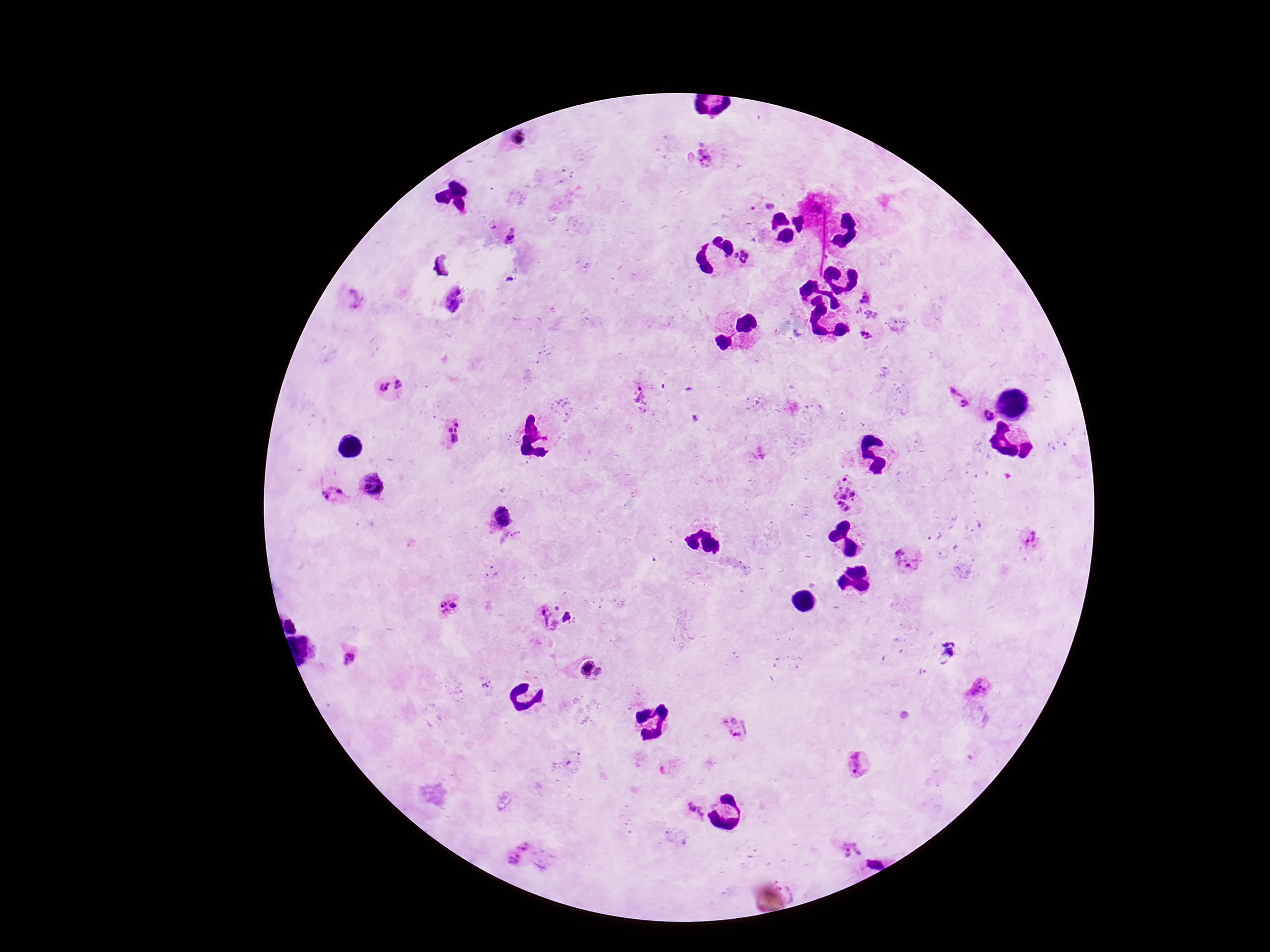
Approximate centers as (x, y) in pixels. Plasmodium parasite locations: (518, 139), (709, 156), (769, 204), (494, 225), (512, 237), (744, 257), (867, 298), (355, 299), (452, 300), (856, 309), (871, 315), (867, 334), (391, 387), (642, 397), (956, 400), (983, 417), (454, 434), (372, 485), (847, 495), (336, 496), (502, 515), (516, 536), (1030, 541), (908, 560), (449, 607), (567, 617), (545, 619), (947, 651), (348, 656), (584, 668), (599, 673), (486, 684), (980, 687), (735, 728), (857, 764), (695, 810), (850, 851), (518, 853). Thick peripheral-blood smear. 100x magnification. Giemsa stain. Image is 1270×952 pixels. Smartphone photograph taken through the microscope eyepiece. Patient malaria status: positive. One field from this slide.